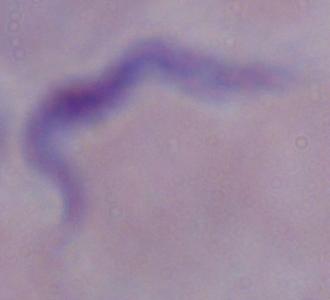 Captured at 1000x magnification. A trypanosome is seen. Photomicrograph.